Describe the morphology of the erythrocytes.
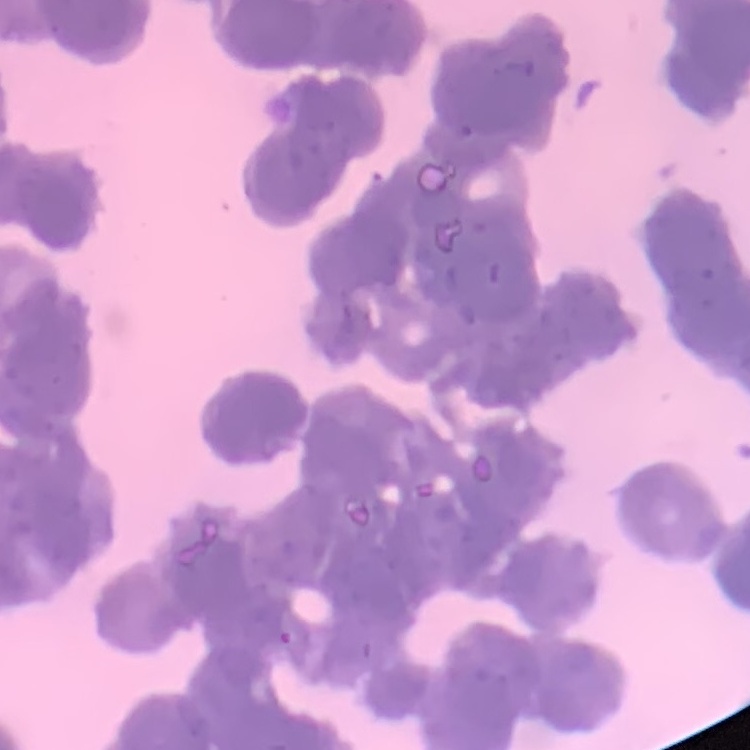
Rouleaux formation.

image type = one tile cut from a larger photomicrograph
preparation = thin blood film
stain = Field's or Giemsa